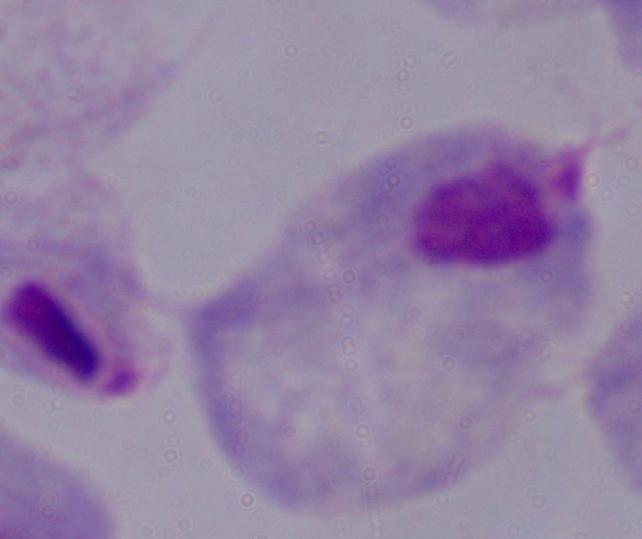 Captured at 1000x magnification. A trichomonad is seen. Micrograph.